Identify the parasite.
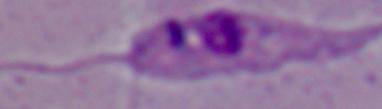
Leishmania.

1000x magnification. Photomicrograph.